Name the parasite shown.
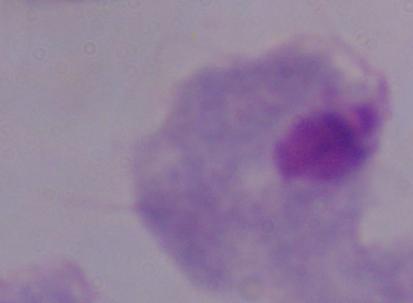
A trichomonad.

Micrograph. Captured at 1000x magnification.